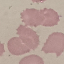

malaria status = uninfected
capture = smartphone through the microscope eyepiece
stain = Giemsa
preparation = thin blood film
image type = automatically extracted cell patch, resized to 64 × 64 pixels